Report the malaria status of this cell.
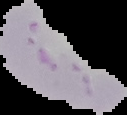
Uninfected.

From a thin blood smear. Cell region segmented out of the field of view; the surrounding area is masked to black. Image is 127×115 pixels.